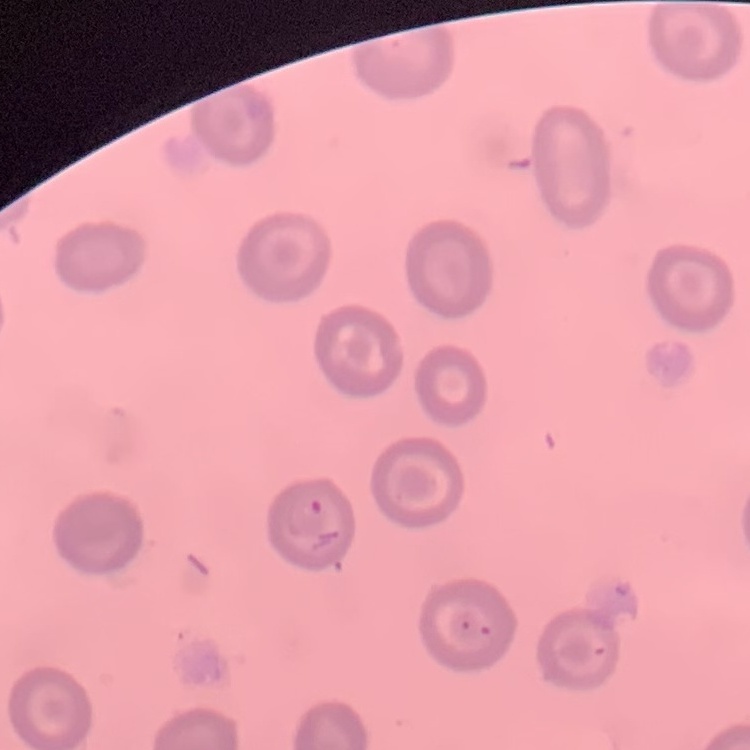

erythrocyte morphology = no rouleaux formation
image type = one tile cut from a larger photomicrograph
preparation = thin blood smear
stain = Field's or Giemsa